Assess the morphology of the red blood cells.
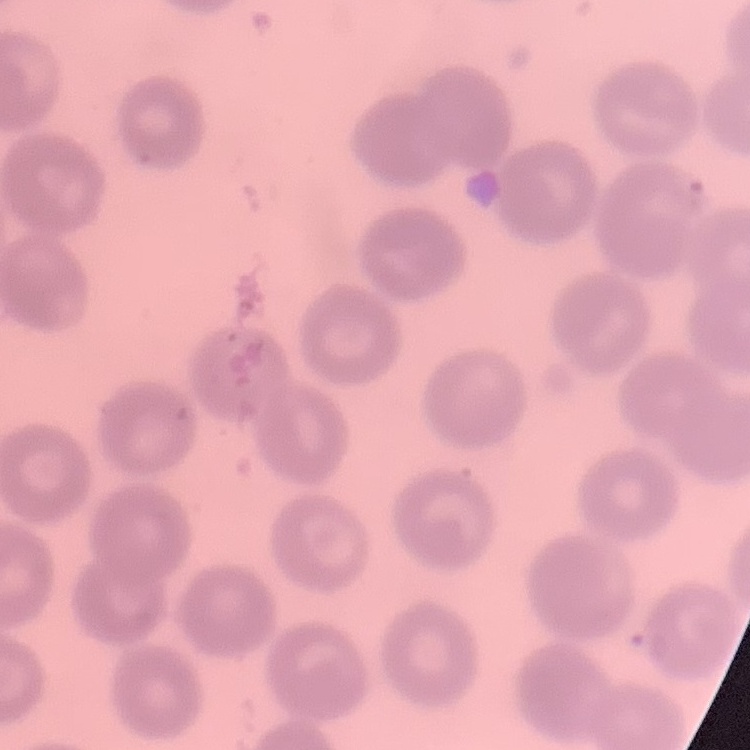

They show no rouleaux formation.

One tile cut from a larger photomicrograph. Thin peripheral smear. Field's or Giemsa stain.